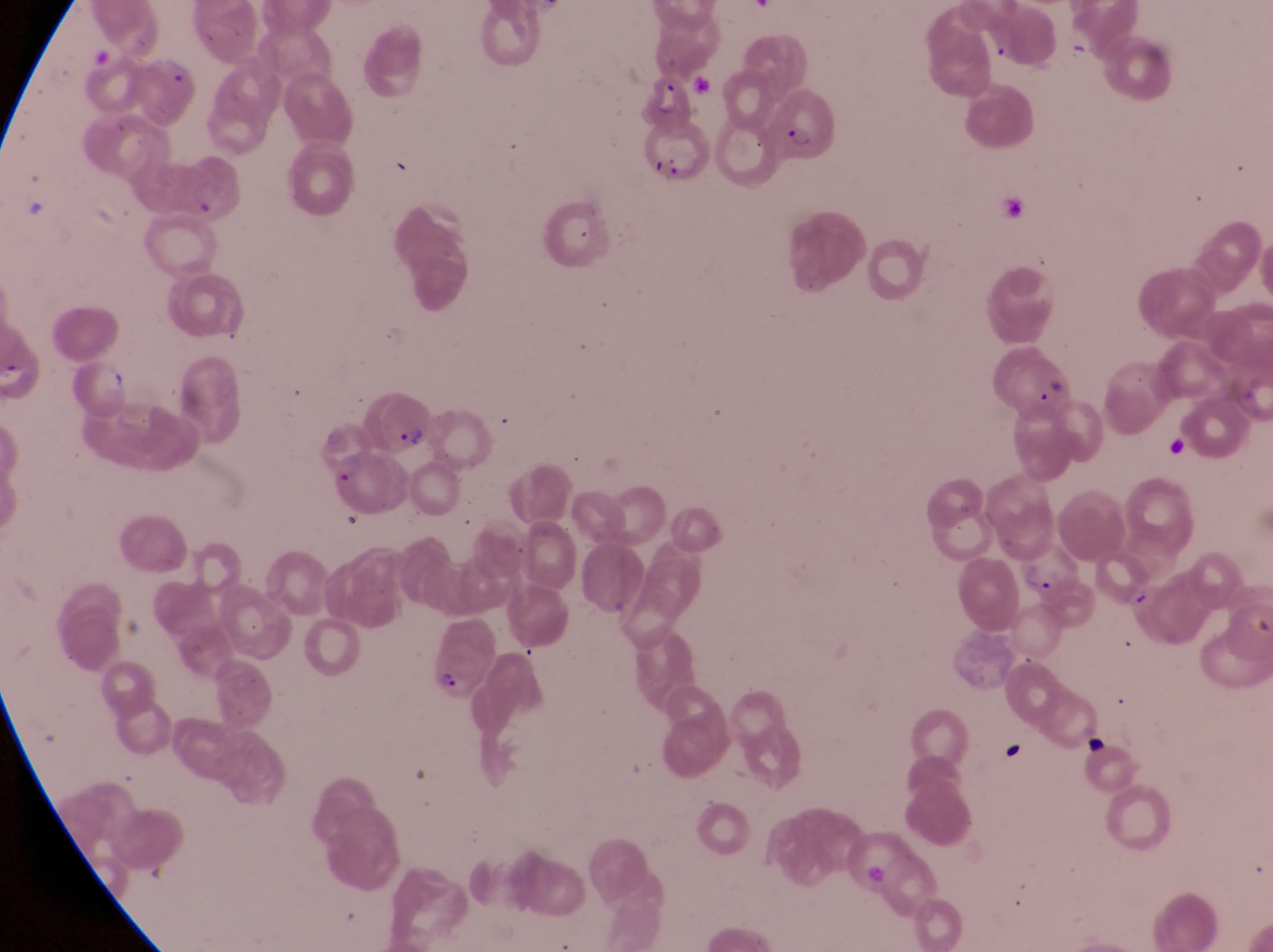
artifact (platelet-like body, stain precipitate, or debris) locations = approximate bounding boxes as {left, top, right, bottom} in pixels: {1163, 432, 1198, 465}, {1078, 724, 1110, 759}, {1001, 739, 1028, 767}
capture = smartphone photograph through the eyepiece of an Olympus CX-23 microscope
image size = 1273×952 pixels
parasitised red blood cell locations = approximate bounding boxes as {left, top, right, bottom} in pixels: {120, 55, 198, 123}, {636, 70, 693, 132}, {771, 83, 838, 165}, {637, 122, 709, 190}, {1006, 340, 1073, 417}, {69, 357, 134, 422}, {357, 390, 434, 457}
magnification = 1000x
country = Uganda
field of view = single
preparation = thin blood film